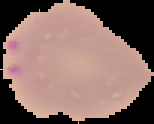
Cell region segmented out of the field of view; the surrounding area is masked to black. Image is 154×124 pixels. Malaria status: parasitized. From a thin blood film.